Give the extent of all Plasmodium falciparum-infected red blood cells.
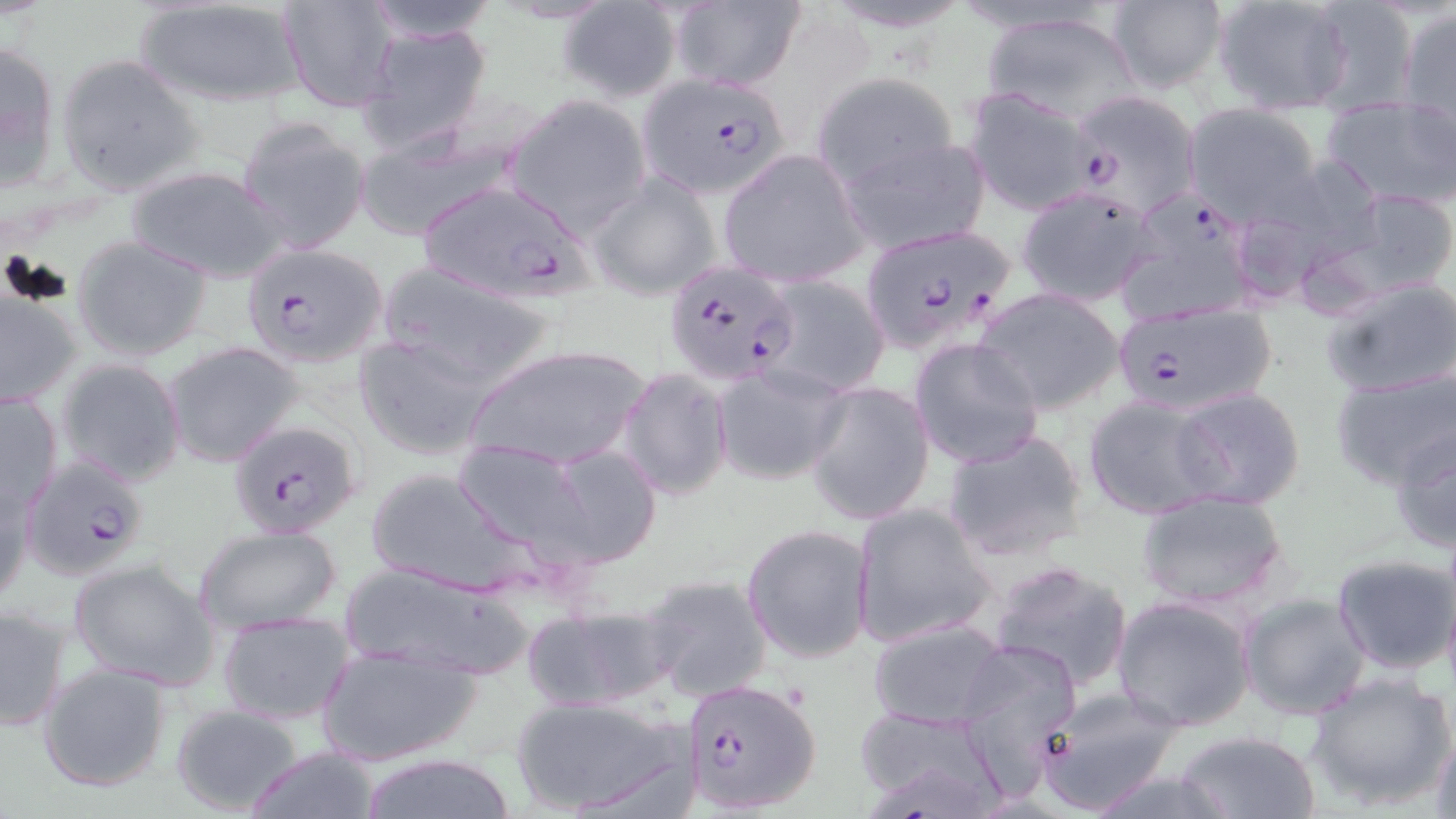

Approximate bounding boxes as [x1, y1, x2, y2] in pixels.
Plasmodium falciparum-infected red blood cells: [637, 72, 797, 199], [1069, 89, 1202, 217], [412, 179, 599, 304], [860, 222, 1019, 353], [240, 242, 386, 368], [664, 258, 802, 387], [1107, 301, 1280, 418], [227, 418, 360, 536], [27, 450, 147, 579], [680, 678, 825, 814].

Uninfected red blood cell locations: [131, 0, 313, 109], [359, 0, 497, 42], [280, 1, 399, 112], [669, 1, 806, 93], [1106, 1, 1228, 95], [1211, 1, 1357, 115], [1300, 1, 1420, 113], [557, 3, 680, 103], [1397, 5, 1455, 121], [979, 11, 1144, 125], [359, 22, 493, 155], [0, 38, 63, 190], [55, 53, 206, 198], [811, 72, 962, 192], [964, 87, 1102, 215], [504, 95, 652, 233], [1322, 98, 1456, 210], [1184, 104, 1323, 223], [235, 117, 370, 255], [351, 120, 523, 243], [839, 134, 993, 254], [718, 148, 868, 287], [1259, 153, 1387, 269], [125, 164, 293, 283], [587, 171, 723, 301], [1015, 186, 1160, 308], [1341, 187, 1456, 297], [1115, 193, 1259, 326], [71, 234, 213, 362], [379, 261, 558, 390], [759, 273, 891, 399], [1321, 276, 1456, 400], [0, 288, 83, 408], [976, 288, 1126, 415], [355, 335, 497, 460], [909, 337, 1045, 469], [163, 341, 305, 467], [464, 343, 650, 474], [56, 358, 186, 486], [709, 364, 849, 486], [1331, 365, 1456, 492], [617, 367, 735, 501], [803, 381, 934, 527], [1169, 386, 1307, 508], [0, 392, 62, 515], [1082, 394, 1222, 518], [1388, 424, 1455, 557], [942, 429, 1090, 564], [452, 438, 596, 562], [538, 442, 663, 569], [367, 468, 526, 594], [1, 472, 36, 605], [1134, 489, 1290, 611], [850, 502, 995, 649], [740, 523, 875, 666], [193, 525, 343, 637], [1332, 553, 1456, 675], [68, 556, 222, 691], [340, 559, 530, 680], [986, 560, 1134, 691], [639, 572, 773, 703], [1237, 592, 1371, 720], [1112, 596, 1256, 733], [524, 601, 674, 713], [0, 604, 72, 733], [216, 611, 354, 724], [868, 619, 1008, 728], [955, 638, 1080, 781], [314, 642, 482, 768], [37, 661, 174, 793], [1306, 674, 1454, 810], [1036, 689, 1184, 814], [513, 696, 691, 817], [170, 704, 305, 814], [853, 707, 1009, 817], [1429, 724, 1456, 819], [1171, 730, 1321, 818], [244, 746, 384, 819], [352, 751, 519, 819]. Slide-level diagnosis: Plasmodium falciparum. Captured at 1000x magnification. May-Grünwald-Giemsa-stained preparation. Single field of view. Optical microscopy. Thin blood smear. Image is 1456×819 pixels.